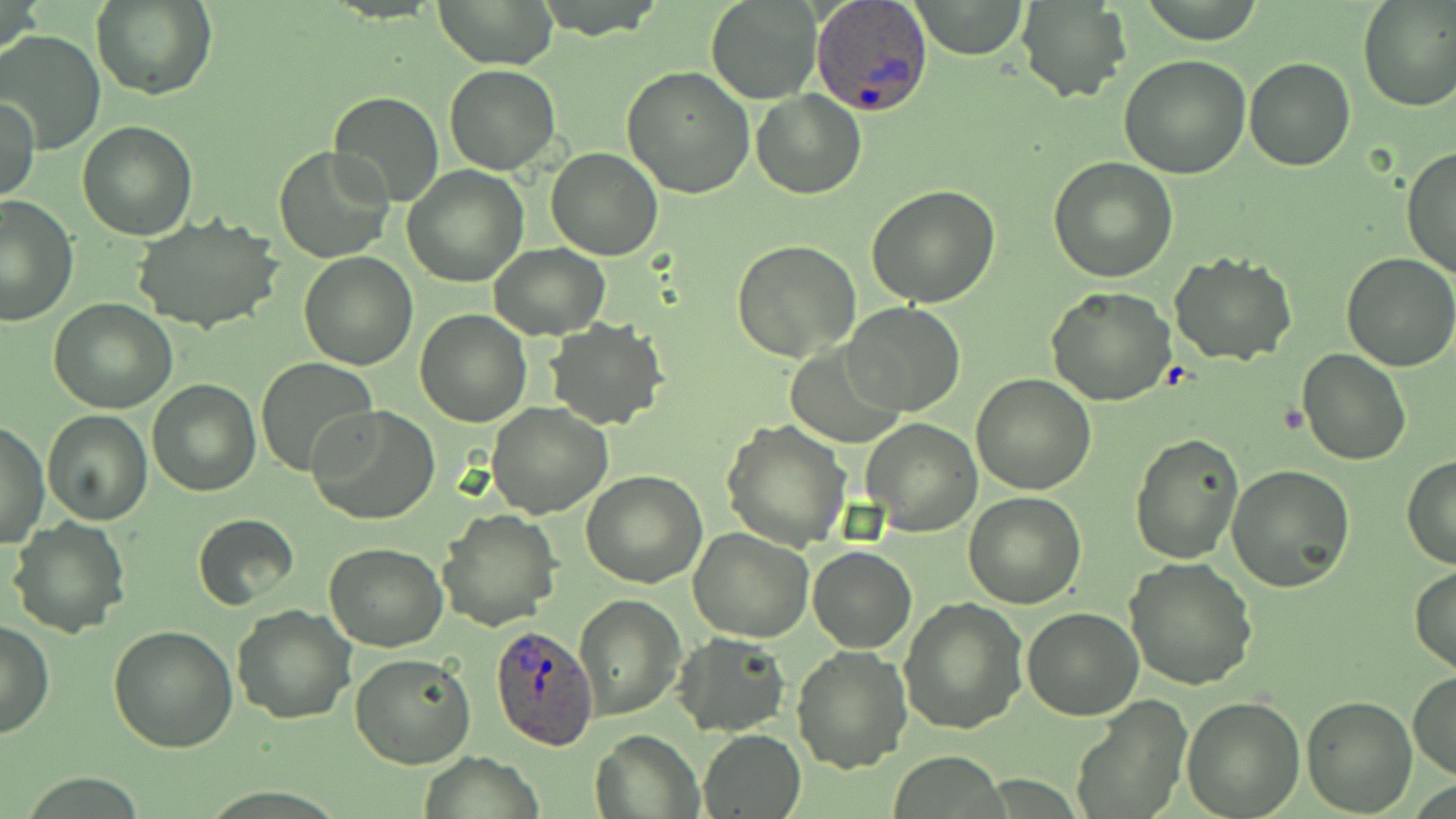

{
  "slide_level_diagnosis": "Plasmodium ovale",
  "modality": "optical microscopy",
  "stain": "May-Grünwald-Giemsa",
  "magnification": "1000x",
  "plasmodium_ovale_infected_red_blood_cell_locations": "approximate bounding boxes as named x1/y1/x2/y2 corners in pixels: (x1=811, y1=0, x2=934, y2=117), (x1=490, y1=623, x2=599, y2=752)",
  "uninfected_red_blood_cell_locations": "approximate bounding boxes as named x1/y1/x2/y2 corners in pixels: (x1=436, y1=0, x2=556, y2=68), (x1=706, y1=0, x2=821, y2=103), (x1=912, y1=0, x2=1026, y2=58), (x1=1357, y1=0, x2=1455, y2=113), (x1=92, y1=1, x2=218, y2=102), (x1=1016, y1=2, x2=1131, y2=102), (x1=0, y1=30, x2=106, y2=154), (x1=1118, y1=55, x2=1251, y2=178), (x1=1243, y1=56, x2=1356, y2=172), (x1=445, y1=65, x2=561, y2=175), (x1=620, y1=66, x2=754, y2=198), (x1=752, y1=89, x2=866, y2=199), (x1=329, y1=91, x2=445, y2=208), (x1=0, y1=95, x2=39, y2=203), (x1=77, y1=121, x2=197, y2=240), (x1=1402, y1=145, x2=1456, y2=283), (x1=274, y1=147, x2=394, y2=262), (x1=545, y1=147, x2=665, y2=260), (x1=1049, y1=155, x2=1179, y2=282), (x1=402, y1=164, x2=529, y2=286), (x1=866, y1=184, x2=1001, y2=308), (x1=0, y1=192, x2=78, y2=328), (x1=132, y1=216, x2=285, y2=334), (x1=732, y1=239, x2=861, y2=362), (x1=488, y1=244, x2=610, y2=340), (x1=299, y1=251, x2=417, y2=369), (x1=1170, y1=252, x2=1296, y2=365), (x1=1339, y1=254, x2=1456, y2=372), (x1=1048, y1=286, x2=1178, y2=406), (x1=48, y1=299, x2=177, y2=413), (x1=842, y1=303, x2=966, y2=417), (x1=413, y1=310, x2=532, y2=428), (x1=546, y1=318, x2=667, y2=430), (x1=788, y1=342, x2=903, y2=448), (x1=1297, y1=347, x2=1411, y2=465), (x1=255, y1=357, x2=377, y2=475), (x1=972, y1=373, x2=1095, y2=494), (x1=148, y1=379, x2=261, y2=496), (x1=309, y1=402, x2=439, y2=525), (x1=486, y1=403, x2=612, y2=518), (x1=42, y1=412, x2=153, y2=526), (x1=861, y1=417, x2=981, y2=537), (x1=722, y1=420, x2=851, y2=553), (x1=1, y1=422, x2=49, y2=550), (x1=1128, y1=433, x2=1243, y2=564), (x1=1402, y1=455, x2=1456, y2=570), (x1=1229, y1=464, x2=1354, y2=591), (x1=581, y1=471, x2=708, y2=588), (x1=962, y1=492, x2=1087, y2=609), (x1=435, y1=507, x2=561, y2=630), (x1=192, y1=513, x2=300, y2=609), (x1=7, y1=517, x2=130, y2=637), (x1=688, y1=527, x2=815, y2=641), (x1=324, y1=543, x2=449, y2=651), (x1=808, y1=546, x2=916, y2=652), (x1=1124, y1=556, x2=1257, y2=690), (x1=1409, y1=566, x2=1456, y2=671), (x1=575, y1=594, x2=683, y2=719), (x1=900, y1=597, x2=1027, y2=734), (x1=230, y1=603, x2=356, y2=725), (x1=1021, y1=608, x2=1144, y2=720), (x1=0, y1=619, x2=53, y2=739), (x1=109, y1=626, x2=239, y2=751), (x1=673, y1=634, x2=791, y2=737), (x1=792, y1=644, x2=911, y2=773), (x1=349, y1=652, x2=475, y2=770), (x1=1408, y1=669, x2=1456, y2=780), (x1=1069, y1=695, x2=1193, y2=817), (x1=1300, y1=696, x2=1416, y2=815), (x1=1182, y1=697, x2=1304, y2=817), (x1=698, y1=729, x2=805, y2=817), (x1=590, y1=730, x2=702, y2=818), (x1=421, y1=751, x2=543, y2=819)",
  "image_size": "1456×819 pixels",
  "field_of_view": "single",
  "preparation": "thin blood smear"
}